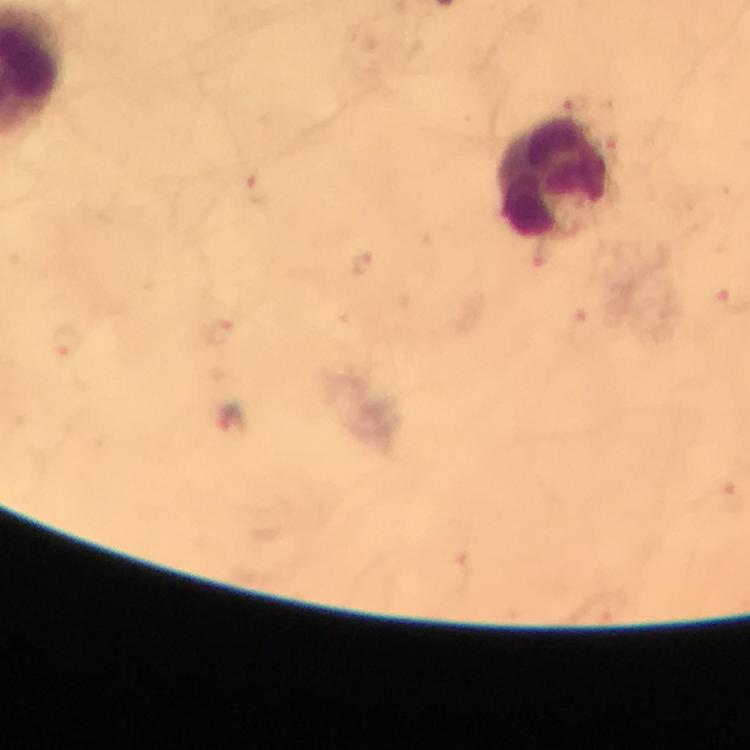

stain = Giemsa
immersion oil = used
magnification = 100x
capture = smartphone mounted on the microscope
cropped from = a single field of view
preparation = thick blood smear
malaria parasite locations = approximate centers as [x, y] in pixels (list possibly incomplete): [575, 103], [615, 150], [260, 190], [542, 255], [363, 267], [590, 330], [222, 331], [66, 344], [229, 417]
image size = 750×750 pixels
leukocyte locations = approximate centers as [x, y] in pixels: [552, 173]
context = from a malaria diagnostic workup